Name the parasite shown.
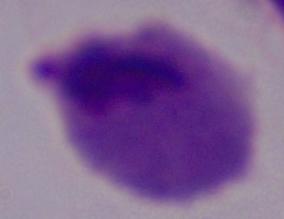

A trichomonad.

Photomicrograph. Captured at 1000x magnification.